Classify this cell by malaria status.
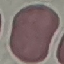
It is uninfected.

stain = Giemsa
preparation = thin blood film
image type = cell patch, automatically extracted from a larger field of view and resized to 64 × 64 pixels
capture = smartphone through the microscope eyepiece